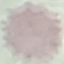
Summary:
  - Result: negative for malaria parasites
  - Stain: Giemsa
  - Image type: cell patch, automatically extracted from a larger field of view and resized to 64 × 64 pixels
  - Preparation: thin blood smear
  - Capture: smartphone through the microscope eyepiece